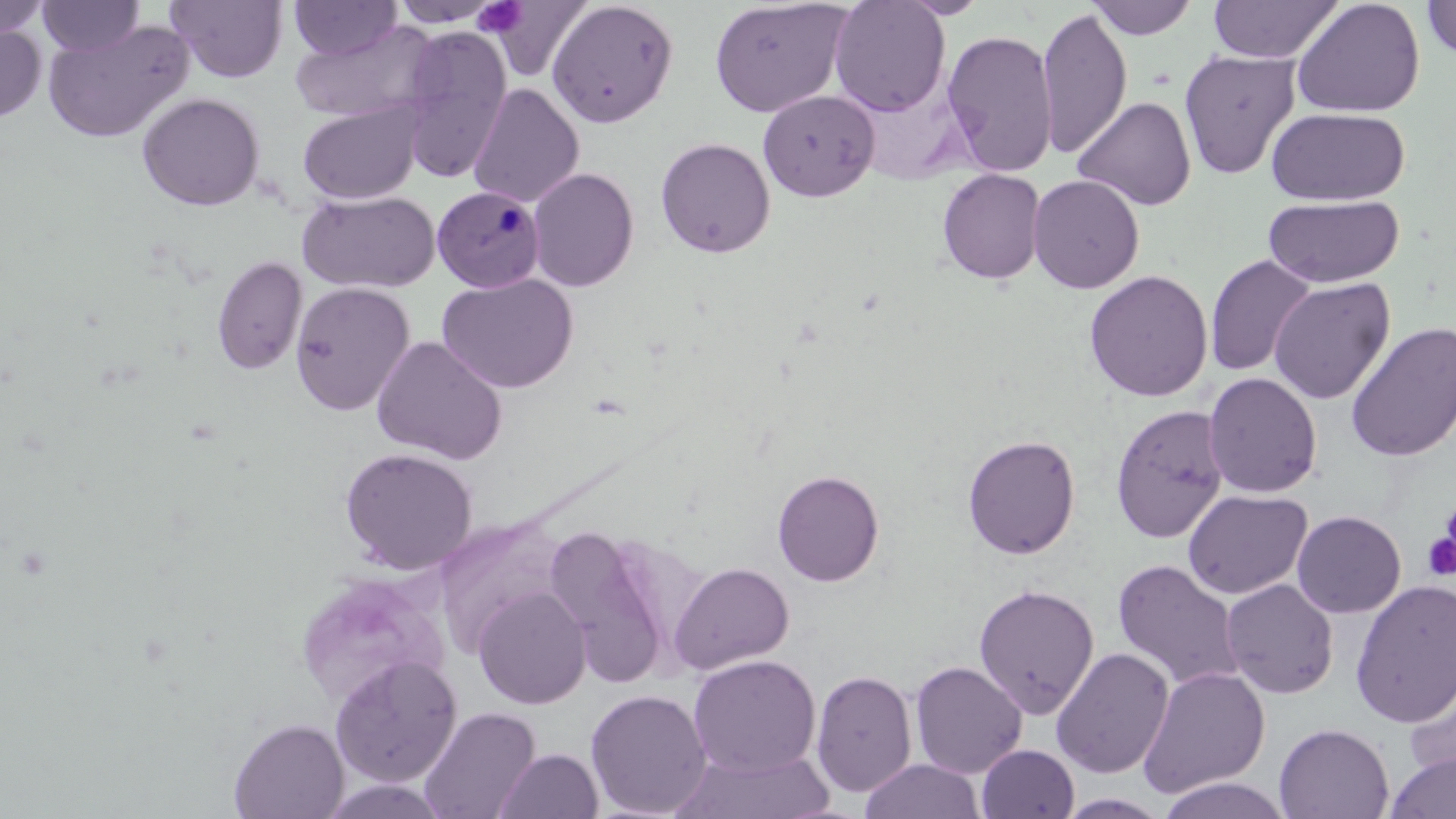

slide-level diagnosis = Plasmodium malariae
field of view = one of a larger specimen
Plasmodium malariae-infected red blood cell locations = approximate bounding boxes as (x1,y1)-(x2,y2) corner pairs in pixels: (432,185)-(544,292)
magnification = 1000x
preparation = thin blood film
uninfected red blood cell locations = approximate bounding boxes as (x1,y1)-(x2,y2) corner pairs in pixels: (0,0)-(50,39), (36,0)-(145,57), (166,0)-(288,83), (390,0)-(505,29), (709,0)-(852,118), (828,0)-(950,116), (900,0)-(989,19), (1086,0)-(1200,39), (1207,0)-(1343,64), (1291,0)-(1426,118), (1421,0)-(1456,61), (289,1)-(400,61), (487,1)-(594,83), (547,2)-(679,128), (1036,6)-(1132,160), (42,18)-(194,144), (289,21)-(438,123), (0,23)-(46,123), (395,28)-(513,185), (941,29)-(1059,177), (1179,50)-(1300,180), (851,80)-(972,185), (468,83)-(584,208), (758,89)-(880,201), (137,92)-(265,211), (1073,96)-(1196,211), (297,100)-(424,204), (1267,107)-(1410,205), (655,136)-(776,258), (528,167)-(640,292), (937,168)-(1046,284), (1028,174)-(1145,294), (298,189)-(440,293), (1263,194)-(1404,288), (1204,254)-(1317,377), (211,255)-(308,375), (1083,269)-(1213,402), (436,273)-(579,394), (1268,277)-(1395,404), (290,282)-(415,417), (1345,321)-(1456,462), (371,336)-(508,465), (1203,372)-(1322,498), (1111,403)-(1230,543), (962,433)-(1081,560), (339,446)-(478,575), (772,469)-(885,587), (1182,489)-(1312,599), (1201,490)-(1327,697), (1292,510)-(1406,618), (542,524)-(685,689), (1112,560)-(1245,692), (668,561)-(794,675), (293,570)-(450,707), (1221,579)-(1339,699), (1350,579)-(1456,728), (973,583)-(1099,719), (472,586)-(591,709), (1050,647)-(1175,779), (688,654)-(821,777), (329,655)-(463,787), (910,660)-(1027,778), (1402,660)-(1456,787), (1137,666)-(1270,798), (810,668)-(917,797), (585,688)-(712,817), (419,706)-(541,819), (228,717)-(349,819), (1274,722)-(1394,819), (976,744)-(1079,819), (495,748)-(603,819), (672,748)-(833,819), (1384,751)-(1456,819), (861,759)-(984,819), (1154,776)-(1293,819), (1056,793)-(1173,819)
platelet locations = approximate bounding boxes as (x1,y1)-(x2,y2) corner pairs in pixels: (473,1)-(527,36), (487,2)-(590,75), (1442,497)-(1456,559), (1421,533)-(1456,581)
modality = light microscopy
image size = 1456×819 pixels
stain = May-Grünwald-Giemsa